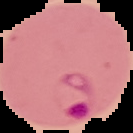
image size = 133×133 pixels
preparation = thin blood smear
malaria status = parasitized
image type = segmented cell region on a black background